Give the extent of all uninfected red blood cells.
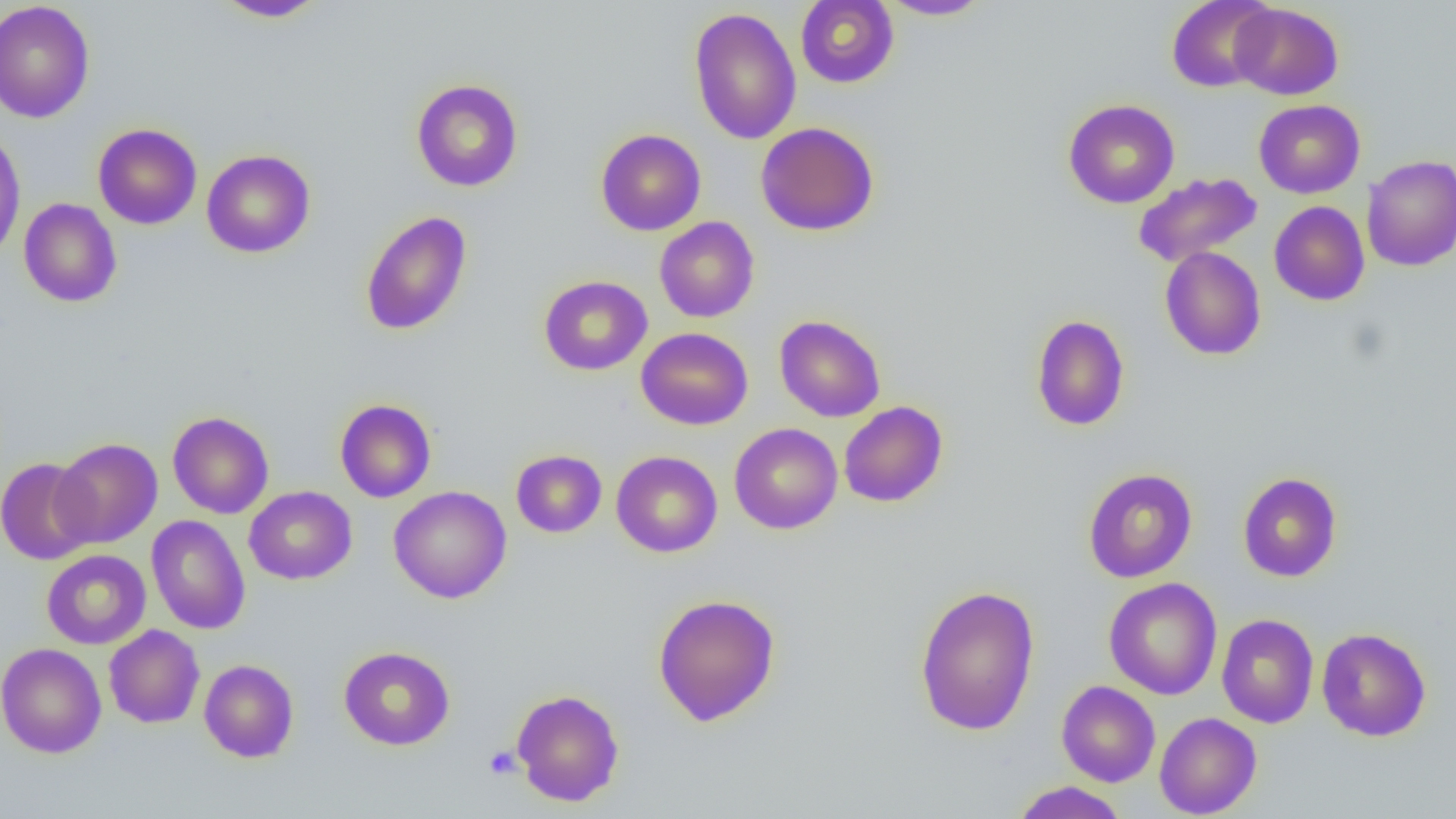
Approximate bounding boxes as (x1,y1)-(x2,y2) corner pairs in pixels.
Uninfected red blood cells: (213,0)-(329,22), (795,0)-(898,88), (877,0)-(993,20), (1166,0)-(1277,93), (0,1)-(96,123), (1230,2)-(1343,100), (688,7)-(802,145), (411,79)-(523,191), (1063,99)-(1180,208), (1253,99)-(1365,198), (755,121)-(879,236), (92,123)-(202,230), (0,128)-(26,263), (595,128)-(706,236), (201,149)-(316,258), (1361,154)-(1456,272), (1133,172)-(1263,267), (19,198)-(122,307), (1269,201)-(1370,306), (359,211)-(472,336), (654,216)-(759,322), (1159,246)-(1266,361), (538,275)-(652,375), (774,314)-(886,422), (1030,314)-(1130,431), (636,327)-(753,430), (335,398)-(436,503), (839,401)-(948,507), (167,411)-(274,519), (729,423)-(843,534), (52,438)-(162,549), (511,449)-(607,538), (611,450)-(723,558), (0,457)-(97,565), (1083,467)-(1198,583), (1095,468)-(1203,699), (1237,471)-(1342,582), (244,486)-(357,585), (388,486)-(512,604), (147,515)-(251,634), (41,549)-(151,649), (1104,578)-(1222,699), (914,584)-(1041,736), (652,593)-(781,726), (1216,613)-(1319,728), (104,624)-(205,728), (1316,627)-(1431,741), (1,642)-(107,758), (339,646)-(455,750), (199,659)-(299,763), (1057,680)-(1160,787), (511,689)-(625,806), (1154,712)-(1262,818), (1011,781)-(1130,819).

Platelet locations: (484,746)-(521,779). Slide-level diagnosis: no evidence of blood parasites. Thin blood smear. One field of a larger specimen. 1000x magnification. Optical microscopy. Image is 1456×819 pixels.